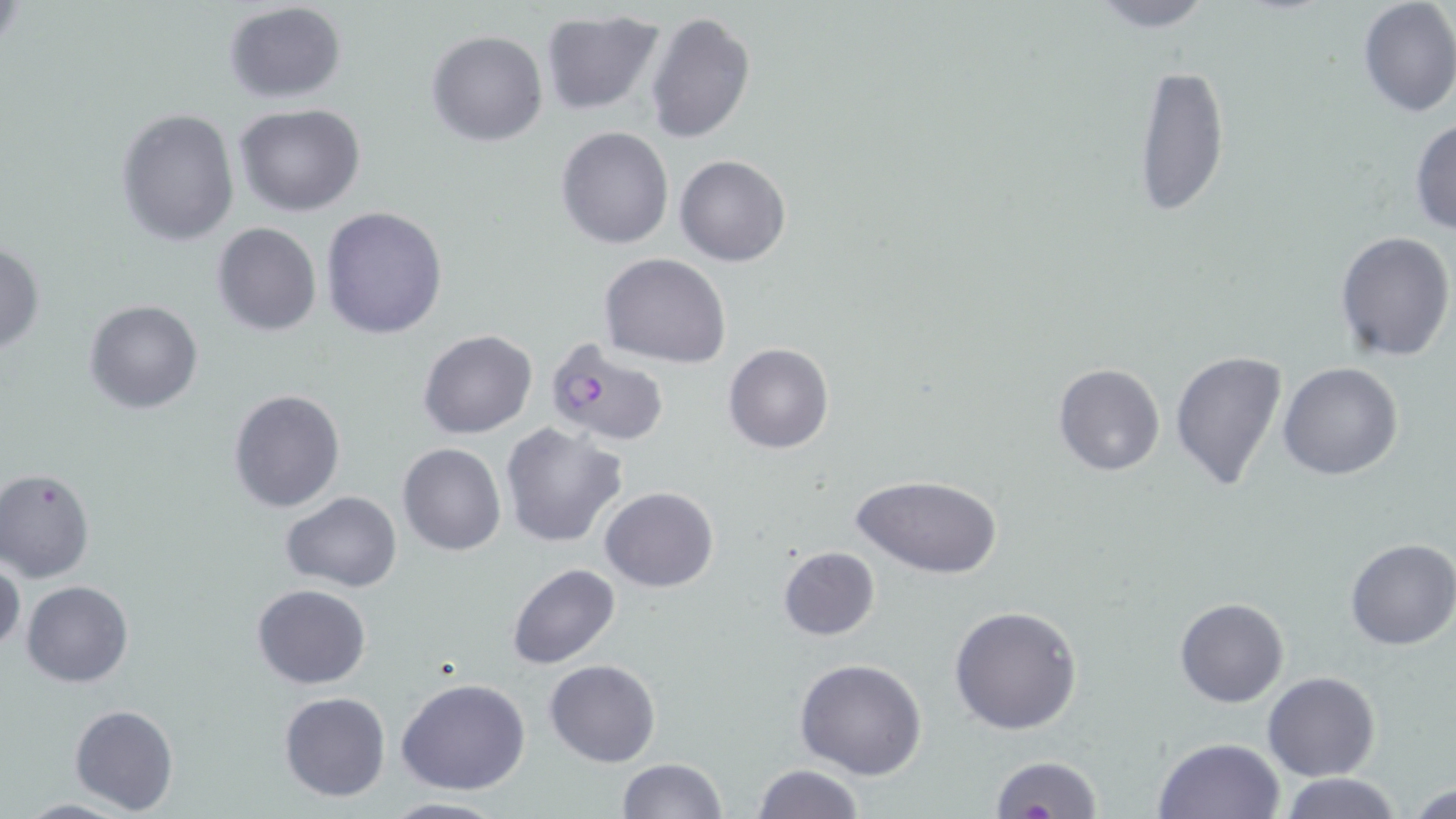
slide_level_diagnosis: Plasmodium falciparum
uninfected_red_blood_cell_locations: 'approximate bounding boxes as (x1,y1)-(x2,y2) corner pairs in pixels: (1082,0)-(1221,32), (1356,0)-(1456,118), (221,1)-(348,104), (541,10)-(665,117), (644,10)-(755,144), (426,28)-(547,146), (1132,62)-(1230,218), (235,104)-(366,217), (116,109)-(239,247), (1408,117)-(1456,236), (556,126)-(673,249), (675,153)-(790,267), (321,205)-(450,340), (211,222)-(322,336), (1334,230)-(1454,361), (0,240)-(46,357), (599,254)-(731,368), (83,299)-(203,416), (417,329)-(537,440), (723,343)-(834,454), (1169,350)-(1288,492), (1052,363)-(1165,478), (1278,363)-(1403,481), (228,389)-(346,514), (499,422)-(628,547), (398,443)-(505,556), (0,468)-(96,582), (854,474)-(1003,579), (601,486)-(718,592), (280,492)-(401,591), (1345,538)-(1456,651), (777,546)-(881,641), (0,556)-(23,657), (505,562)-(621,671), (22,580)-(132,688), (252,583)-(372,689), (1175,596)-(1289,707), (949,604)-(1083,736), (795,657)-(928,780), (544,659)-(662,767), (1263,670)-(1380,781), (396,678)-(531,795), (279,691)-(390,803), (70,704)-(179,814), (1152,736)-(1285,818), (987,754)-(1102,818), (615,758)-(726,819), (751,763)-(865,818), (1278,774)-(1404,819), (1406,780)-(1455,818), (379,794)-(509,818), (12,798)-(138,818)'
stain: May-Grünwald-Giemsa
image_size: 1456×819 pixels
plasmodium_falciparum_infected_red_blood_cell_locations: 'approximate bounding boxes as (x1,y1)-(x2,y2) corner pairs in pixels: (539,335)-(672,447)'
modality: light microscopy
field_of_view: one of a larger specimen
preparation: thin blood film
magnification: 1000x